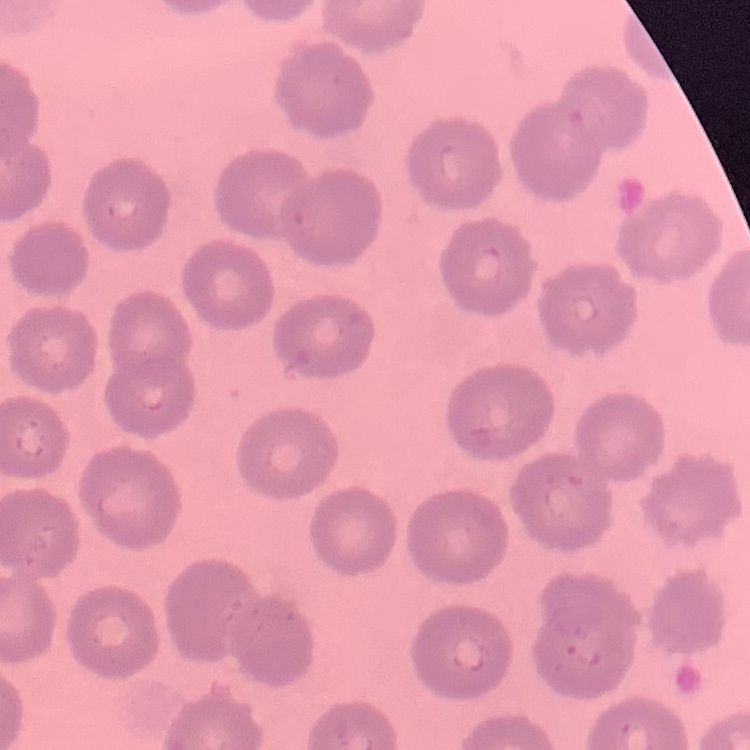

{
  "erythrocyte_morphology": "no rouleaux formation",
  "preparation": "thin blood film",
  "image_type": "square crop of a larger photomicrograph",
  "stain": "Field's or Giemsa"
}